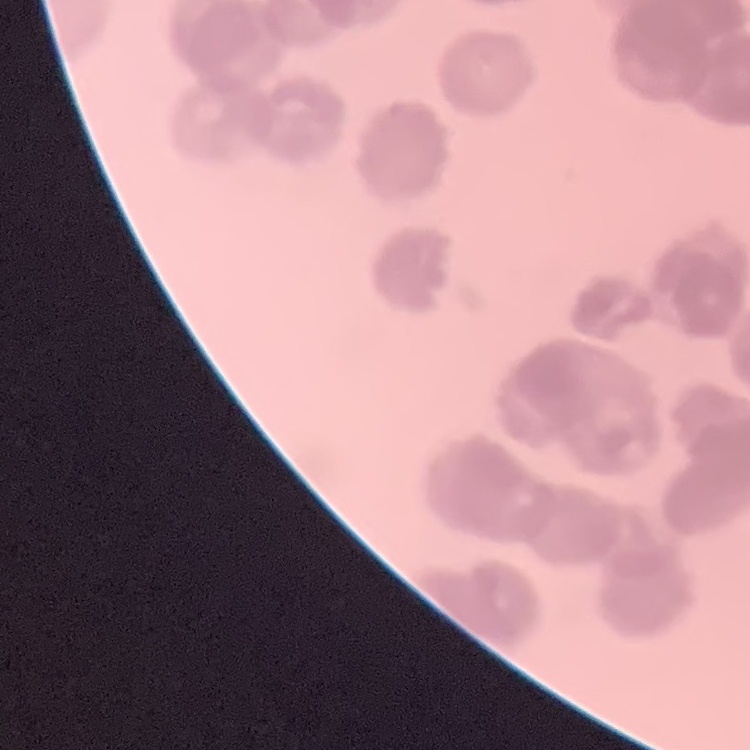
Summary:
  - Red blood cell morphology: rouleaux formation
  - Preparation: thin blood film
  - Image type: square crop of a larger photomicrograph
  - Stain: Field's or Giemsa